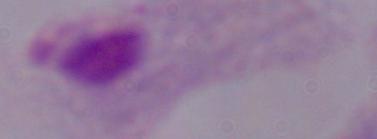
A trichomonad is shown. 1000x magnification. Micrograph.